Classify this cell by malaria status.
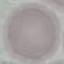

Uninfected.

Automatically extracted cell patch, resized to 64 × 64 pixels. Giemsa stain. Thin blood film. Acquired by smartphone through the microscope eyepiece.